Assess the morphology of the red blood cells.
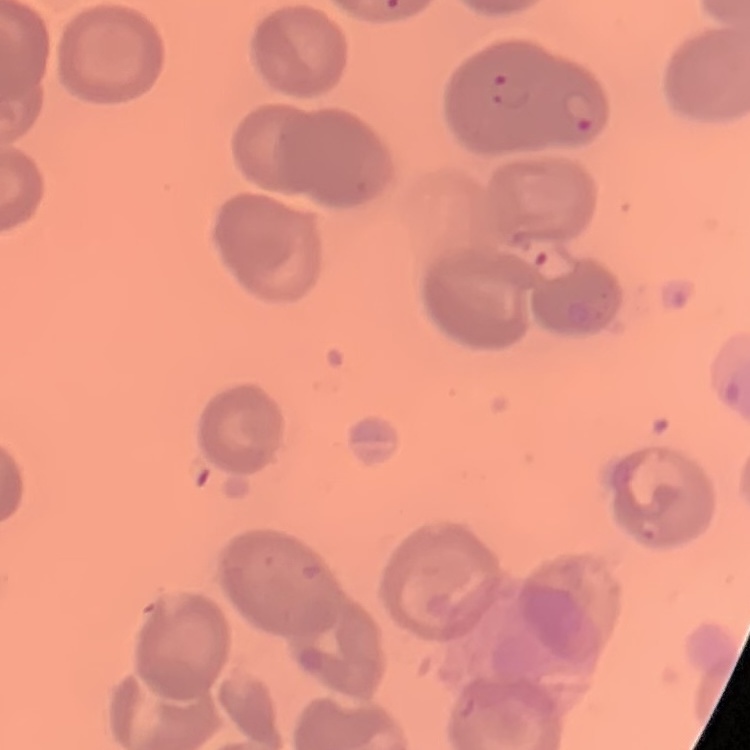

They show no rouleaux formation.

stain: Field's or Giemsa
image_type: one tile cut from a larger photomicrograph
preparation: thin peripheral smear